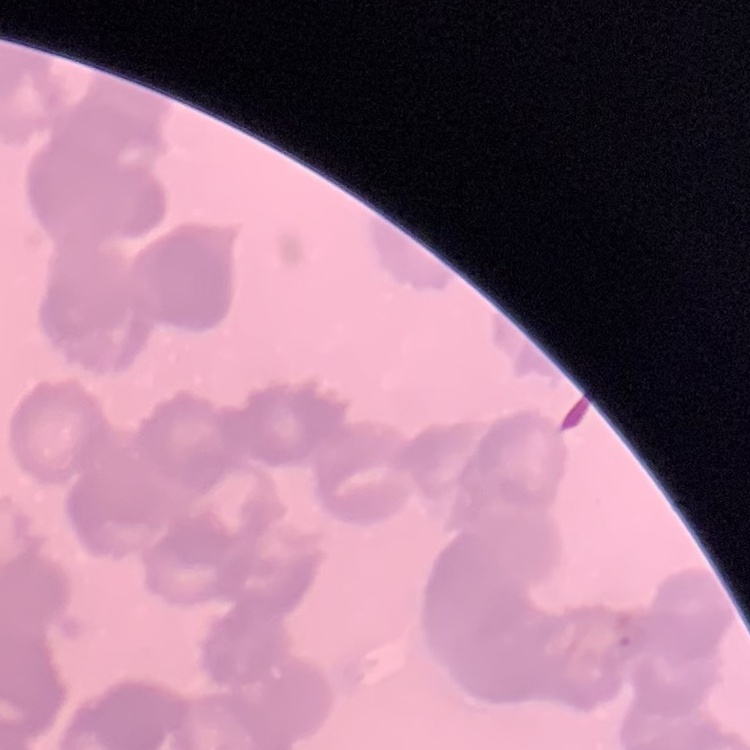

The erythrocytes exhibit rouleaux formation. Thin blood smear. Square crop of a larger photomicrograph. Stained with either Field's or Giemsa.